Classify this cell by malaria status.
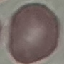
Uninfected.

capture = smartphone through the microscope eyepiece
image type = automatically extracted cell patch, resized to 64 × 64 pixels
stain = Giemsa
preparation = thin blood smear